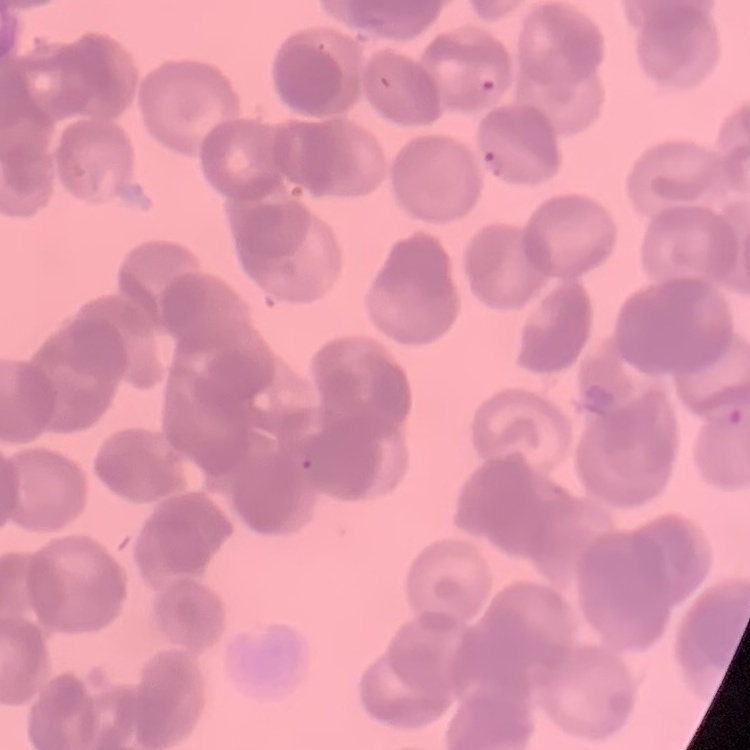
Summary:
  - Erythrocyte morphology: rouleaux formation
  - Image type: one tile cut from a larger photomicrograph
  - Preparation: thin blood film
  - Stain: Field's or Giemsa